Report the malaria status of this cell.
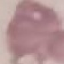

Uninfected.

Automatically extracted cell patch, resized to 64 × 64 pixels. Thin blood film. Giemsa stain. Photographed with a smartphone camera at the microscope eyepiece.